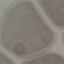

Summary:
  - Malaria status: uninfected
  - Capture: smartphone camera at the microscope eyepiece
  - Image type: cell patch, automatically extracted from a larger field of view and resized to 64 × 64 pixels
  - Preparation: thin blood smear
  - Stain: Giemsa